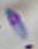
modality = micrograph
identification = Toxoplasma gondii
magnification = 1000x